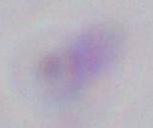
Summary:
  - Identification: Toxoplasma gondii
  - Modality: photomicrograph
  - Magnification: 1000x